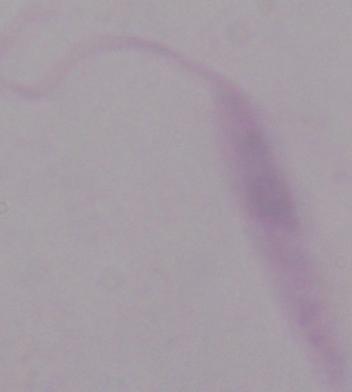
1000x magnification. A Leishmania parasite is shown. Photomicrograph.